Comment on the morphology of the red blood cells.
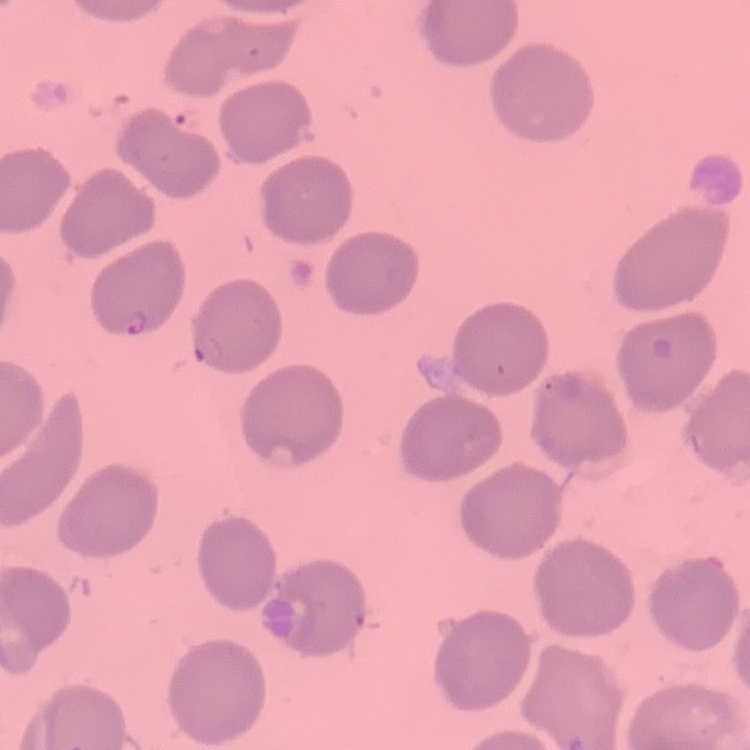

They show no rouleaux formation.

Summary:
  - Preparation: thin peripheral smear
  - Stain: Field's or Giemsa
  - Image type: square crop of a larger photomicrograph